Report the malaria status of this cell.
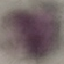
It is uninfected.

Photographed with a smartphone camera at the microscope eyepiece. Giemsa-stained preparation. Thin smear of blood. Cell patch, automatically extracted from a larger field of view and resized to 64 × 64 pixels.